State the blood parasite species.
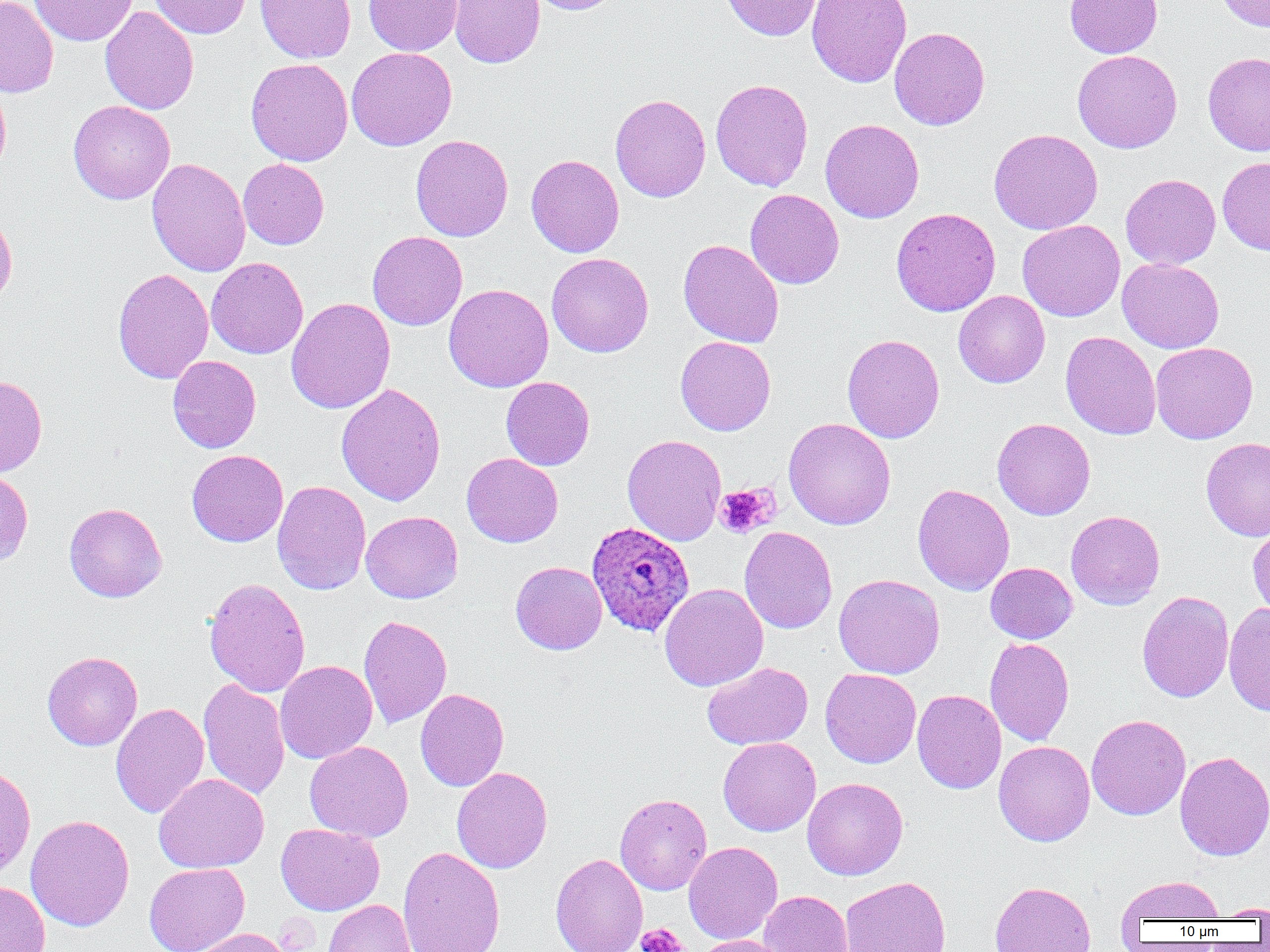
Plasmodium ovale.

Approximate bounding boxes as (x1, y1, x2, y2) in pixels. Platelet locations: (715, 484, 778, 538), (636, 923, 689, 952). Plasmodium ovale-infected red blood cell locations: (586, 521, 695, 636). Uninfected red blood cell locations: (0, 0, 59, 97), (29, 0, 138, 46), (150, 0, 251, 39), (255, 0, 356, 63), (364, 0, 462, 56), (448, 0, 545, 68), (526, 0, 620, 15), (720, 0, 823, 41), (1065, 0, 1163, 58), (1215, 0, 1270, 32), (807, 1, 912, 88), (100, 6, 199, 115), (889, 27, 990, 130), (346, 47, 457, 151), (1072, 49, 1182, 153), (1203, 51, 1270, 156), (246, 58, 353, 166), (710, 78, 813, 192), (0, 80, 11, 179), (609, 93, 711, 203), (68, 101, 175, 204), (820, 119, 924, 223), (988, 129, 1103, 235), (411, 134, 513, 242), (526, 154, 624, 258), (1218, 156, 1270, 255), (147, 157, 250, 277), (238, 159, 329, 249), (1120, 173, 1221, 269), (745, 188, 844, 289), (0, 208, 17, 309), (891, 208, 1001, 316), (1017, 220, 1125, 321), (367, 231, 467, 331), (678, 239, 784, 348), (546, 253, 653, 357), (206, 257, 308, 359), (1117, 257, 1224, 354), (112, 268, 214, 384), (443, 283, 554, 392), (953, 290, 1050, 388), (286, 297, 395, 414), (1060, 331, 1161, 440), (842, 334, 945, 443), (675, 336, 776, 436), (1151, 342, 1258, 444), (168, 355, 261, 453), (0, 375, 47, 477), (501, 377, 595, 470), (336, 383, 446, 506), (783, 418, 896, 530), (992, 418, 1095, 520), (622, 434, 726, 546), (1201, 438, 1270, 541), (186, 449, 288, 547), (461, 453, 563, 547), (0, 468, 33, 568), (272, 480, 371, 595), (912, 483, 1015, 595), (64, 503, 167, 602), (1065, 510, 1165, 610), (361, 511, 463, 603), (1247, 523, 1270, 622), (739, 526, 837, 634), (510, 561, 607, 655), (985, 562, 1077, 643), (833, 574, 945, 679), (203, 577, 311, 698), (659, 582, 768, 691), (1137, 590, 1234, 702), (1224, 601, 1270, 717), (358, 614, 452, 729), (985, 636, 1074, 747), (42, 651, 143, 750), (275, 660, 378, 764), (702, 661, 813, 750), (820, 668, 921, 768), (198, 678, 290, 800), (415, 688, 509, 791), (912, 689, 1006, 793), (110, 702, 209, 818), (1086, 714, 1190, 820), (718, 737, 821, 836), (993, 740, 1095, 846), (305, 741, 413, 842), (1174, 751, 1270, 861), (0, 762, 36, 879), (452, 767, 553, 873), (154, 773, 269, 873), (802, 777, 907, 880), (615, 793, 712, 895), (25, 814, 135, 931), (276, 823, 385, 915), (683, 841, 782, 944), (397, 846, 505, 952), (550, 853, 648, 952), (144, 863, 249, 952), (1115, 875, 1225, 923), (839, 876, 951, 952), (0, 881, 50, 952), (989, 881, 1096, 952), (759, 890, 853, 952), (324, 899, 416, 952), (1212, 902, 1270, 919), (187, 928, 292, 952), (692, 935, 792, 952). Captured at 1000x magnification. Single field of view. Thin blood film. Image is 1270×952 pixels. Optical microscopy.